Assess this cell for malaria.
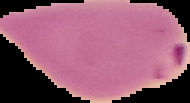
It is parasitized.

{
  "image_type": "segmented cell region with the area outside set to black",
  "preparation": "thin blood film",
  "image_size": "190×103 pixels"
}